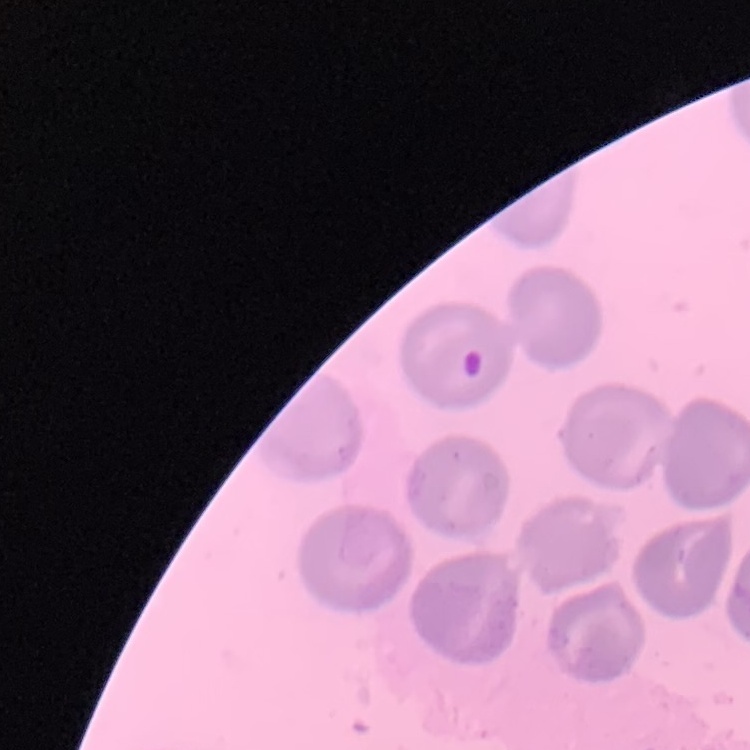
The red blood cells show no rouleaux formation. Thin peripheral smear. Stained with either Field's or Giemsa. One tile cut from a larger photomicrograph.